Assess this cell for malaria.
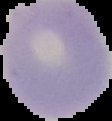
Uninfected.

image_type: cell region segmented out of the field of view; surrounding area masked to black
preparation: thin blood smear
image_size: 112×121 pixels